Identify the cell.
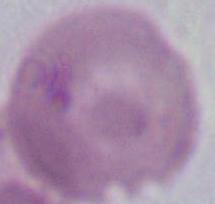
This is an erythrocyte.

modality = photomicrograph
magnification = 1000x